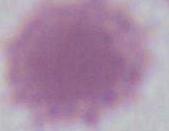
{
  "modality": "micrograph",
  "magnification": "1000x",
  "identification": "erythrocyte"
}